Assess this cell for malaria.
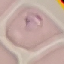

Parasitized.

Giemsa-stained preparation. Acquired by smartphone through the microscope eyepiece. Thin blood film. Cell patch, automatically extracted from a larger field of view and resized to 64 × 64 pixels.